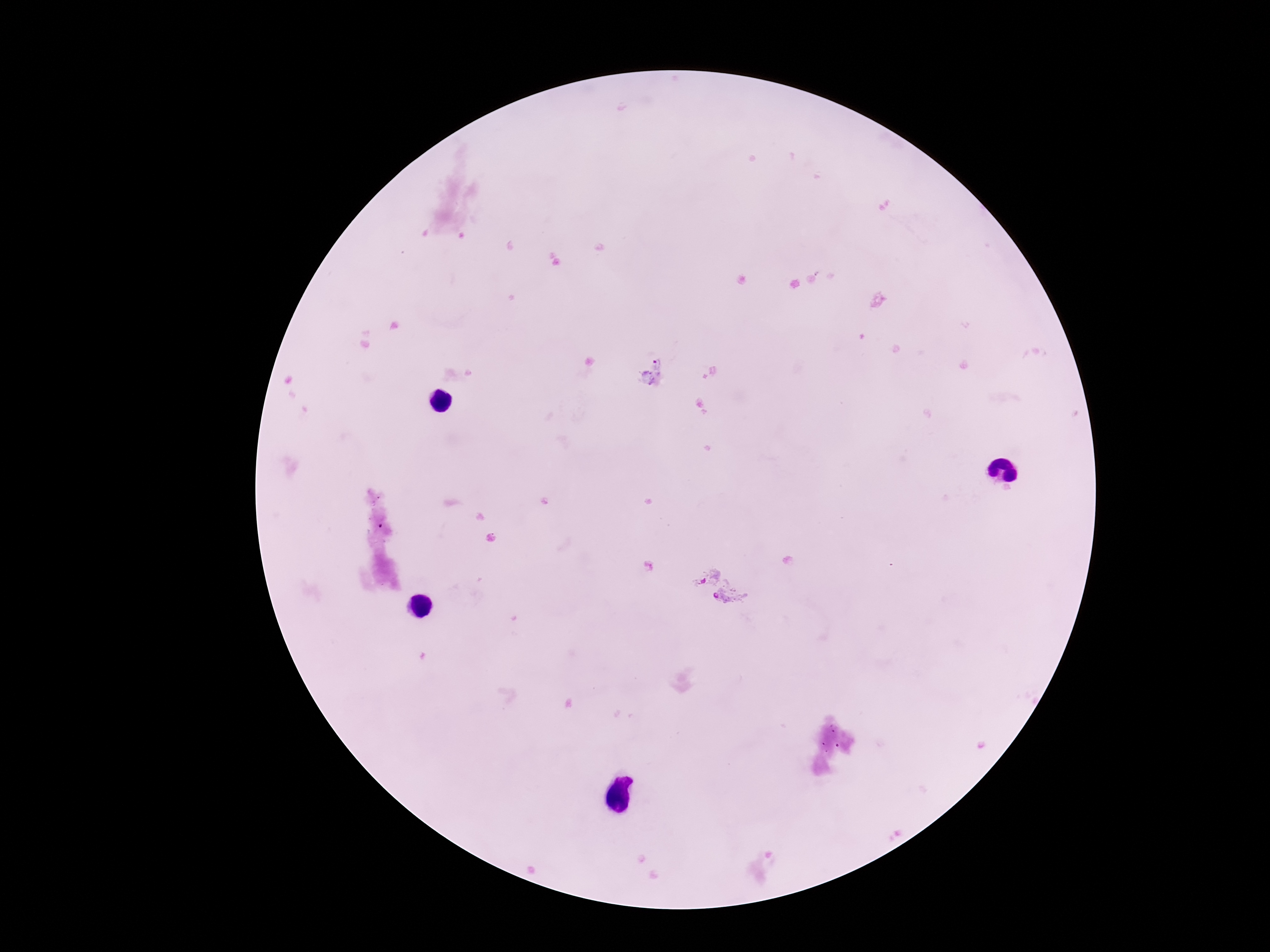
Approximate object centers, in pixels from the top-left corner.
Summary:
  - Plasmodium parasite locations: (x=652, y=373), (x=704, y=575), (x=731, y=598)
  - Magnification: 100x
  - Stain: Giemsa
  - Preparation: thick peripheral-blood smear
  - Patient malaria status: positive
  - Capture: smartphone camera through the microscope eyepiece
  - Image size: 1270×952 pixels
  - Field of view: one from this slide